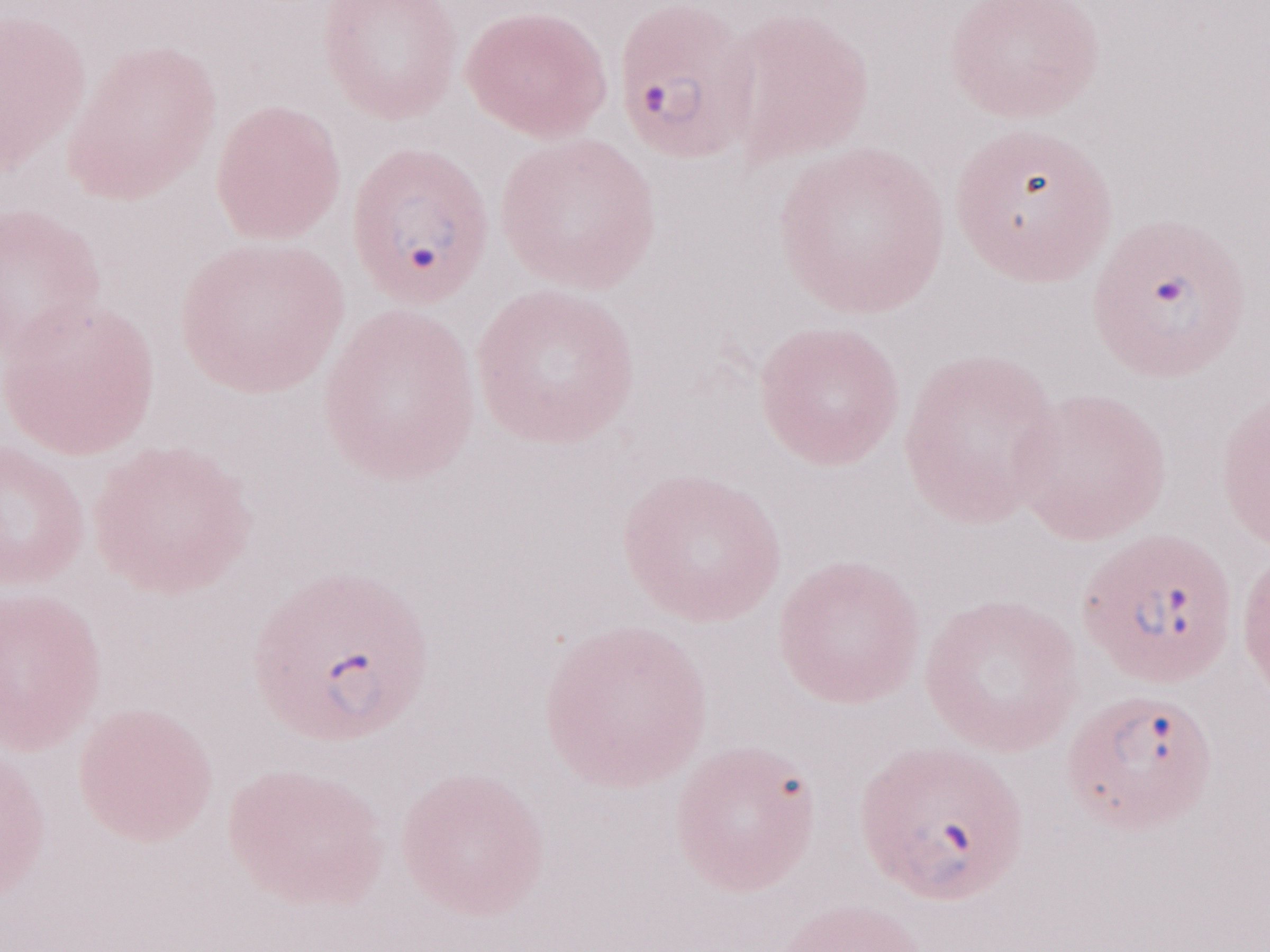

Single field of view. May-Grünwald-Giemsa-stained preparation. 1,000x magnification. Malaria diagnosis (patient-level): positive. Image is 1270×952 pixels. Thin blood smear. Olympus BX43 microscope and DP73 digital camera.